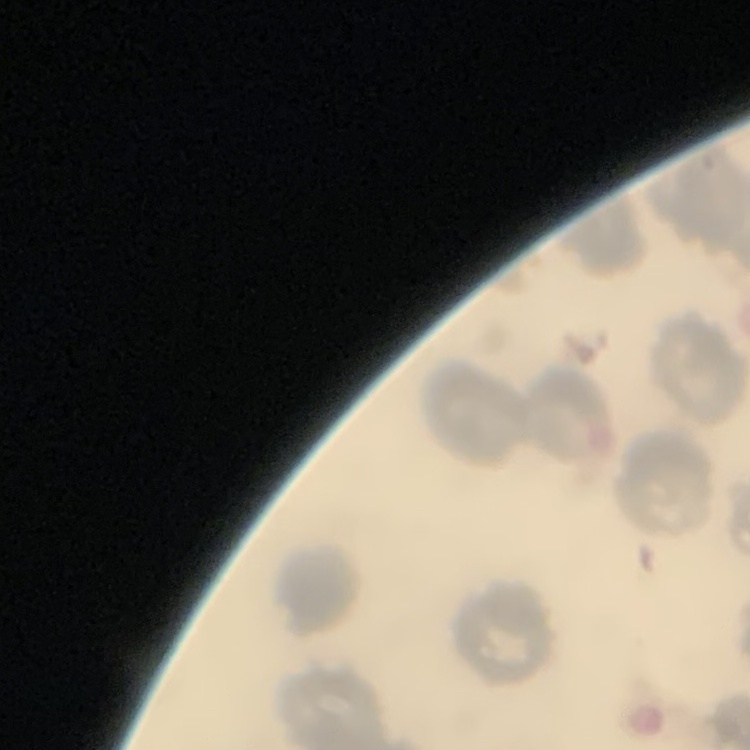
red_blood_cell_morphology: no rouleaux formation
image_type: square crop of a larger photomicrograph
stain: Field's or Giemsa
preparation: thin blood film